Identify the parasite.
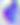

This is Toxoplasma gondii.

modality: micrograph
magnification: 400x